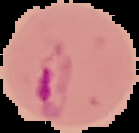

Summary:
  - Image size: 139×133 pixels
  - Preparation: thin blood smear
  - Malaria status: parasitized
  - Image type: segmented cell region on a black background